Locate every blood parasite and identify its species.
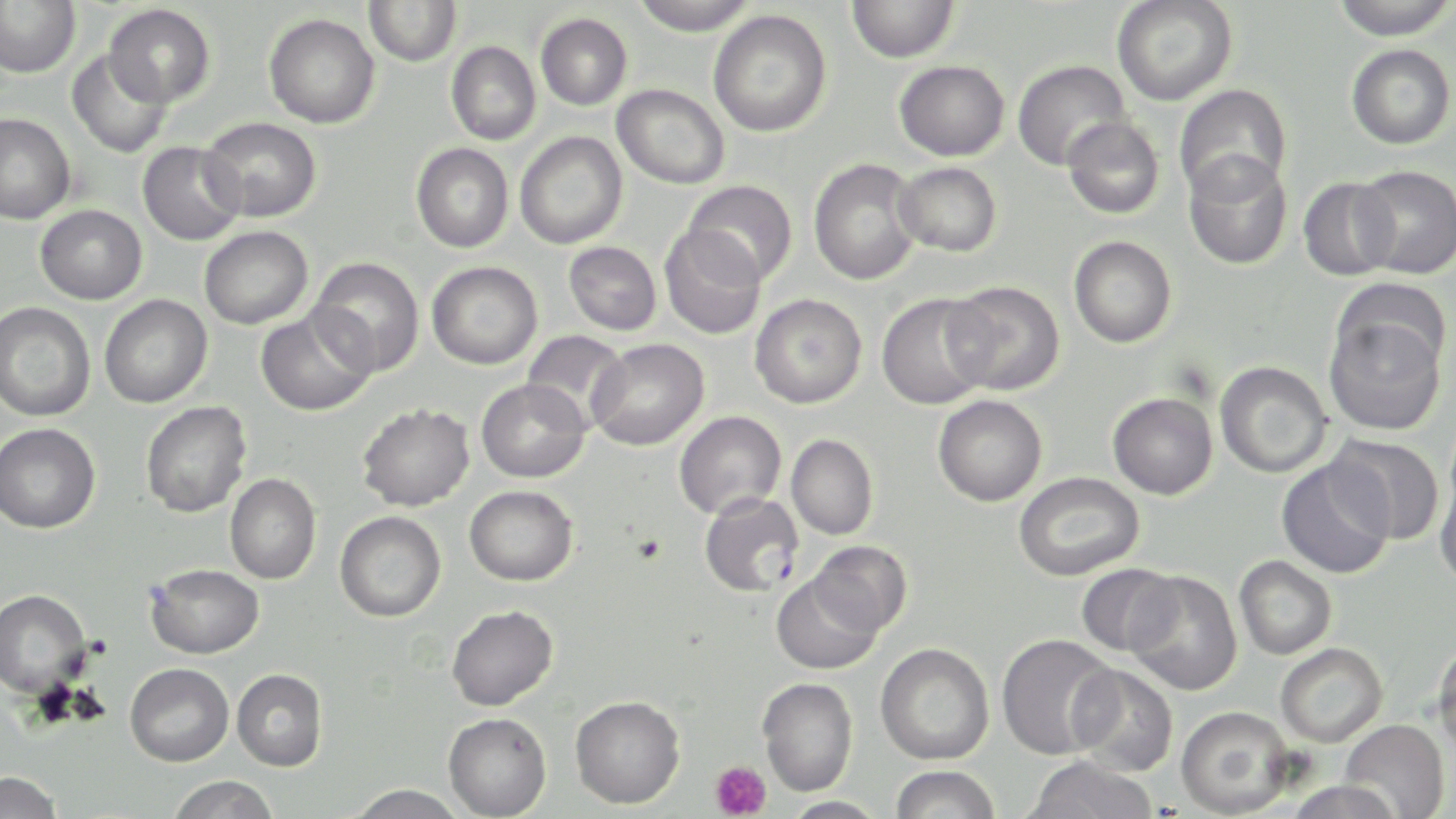

Approximate bounding boxes as (x1,y1)-(x2,y2) corner pairs in pixels.
Plasmodium falciparum-infected red blood cells: (699,493)-(804,597).
No Plasmodium ovale, Plasmodium malariae, Plasmodium vivax, Babesia divergens, or Trypanosoma brucei observed.

Summary:
  - Platelet locations: (709,760)-(772,819)
  - Uninfected red blood cell locations: (0,0)-(80,79), (630,0)-(759,36), (847,0)-(960,63), (1111,0)-(1238,106), (1328,0)-(1456,40), (364,1)-(462,67), (104,4)-(215,107), (708,10)-(832,137), (264,13)-(380,129), (536,13)-(632,110), (446,41)-(541,145), (1346,44)-(1455,149), (67,49)-(172,159), (1012,59)-(1131,171), (894,60)-(1009,161), (612,84)-(730,189), (1173,84)-(1292,201), (0,113)-(75,224), (199,116)-(322,222), (1061,116)-(1165,220), (514,131)-(628,249), (137,141)-(246,246), (411,143)-(514,252), (1183,152)-(1292,270), (808,159)-(923,286), (893,162)-(1002,257), (1352,165)-(1456,279), (1298,177)-(1401,281), (682,179)-(798,286), (35,204)-(147,304), (199,226)-(312,329), (659,226)-(766,340), (1068,236)-(1178,348), (563,241)-(662,335), (309,257)-(424,377), (427,261)-(542,369), (943,281)-(1065,395), (877,293)-(994,410), (99,294)-(213,408), (750,294)-(867,409), (1,302)-(95,422), (1324,308)-(1447,436), (255,310)-(376,416), (521,330)-(631,431), (588,338)-(709,451), (1215,361)-(1333,478), (476,378)-(590,483), (1107,392)-(1218,500), (932,395)-(1047,507), (140,401)-(251,518), (357,403)-(474,511), (674,410)-(786,520), (0,423)-(101,533), (786,434)-(879,540), (1329,434)-(1445,545), (1276,458)-(1396,579), (1434,464)-(1456,592), (1013,471)-(1144,581), (224,473)-(321,584), (464,485)-(578,586), (335,511)-(446,622), (809,540)-(914,635), (1234,555)-(1337,660), (146,564)-(264,659), (1076,564)-(1182,656), (1124,571)-(1242,695), (771,572)-(884,674), (0,589)-(91,697), (446,605)-(558,711), (996,633)-(1119,759), (1431,638)-(1456,759), (875,642)-(995,764), (1275,642)-(1388,747), (125,663)-(233,766), (1067,663)-(1179,776), (232,668)-(328,771), (758,678)-(858,796), (570,695)-(685,809), (1175,705)-(1296,818), (443,712)-(552,818), (1340,718)-(1450,819), (1023,756)-(1159,819), (890,765)-(1000,819), (0,770)-(64,819), (167,775)-(280,819), (1287,779)-(1404,819), (347,783)-(468,819), (780,796)-(889,818)
  - Slide-level diagnosis: Plasmodium falciparum
  - Image size: 1456×819 pixels
  - Magnification: 1000x
  - Stain: May-Grünwald-Giemsa
  - Preparation: thin blood smear
  - Field of view: single
  - Modality: light microscopy